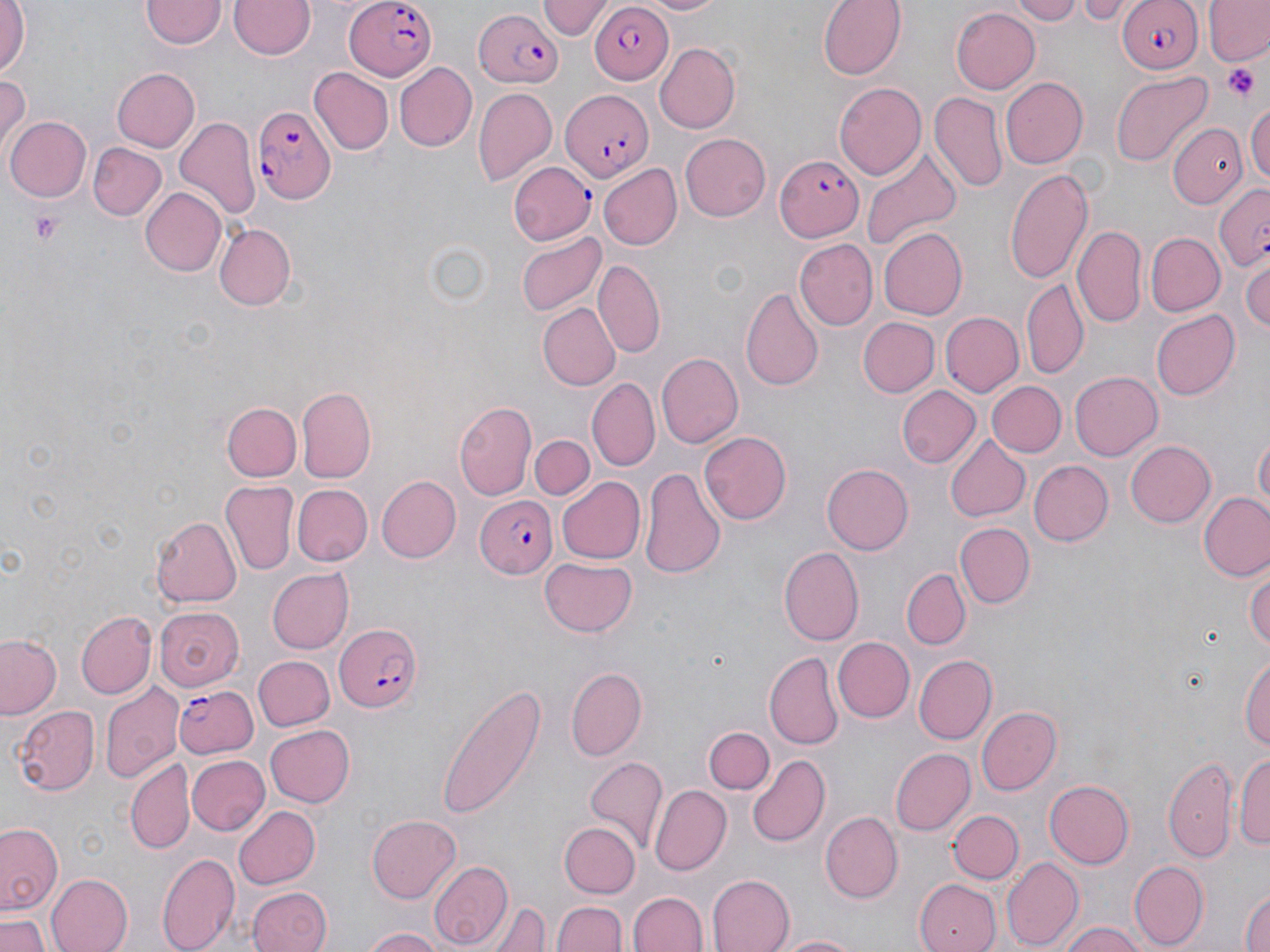
Approximate bounding boxes as (x1,y1)-(x2,y2) corner pairs in pixels. Plasmodium falciparum-infected red blood cell locations: (345,0)-(438,80), (1114,0)-(1203,74), (588,5)-(671,84), (473,8)-(563,90), (560,91)-(653,179), (252,107)-(336,204), (774,155)-(862,241), (508,163)-(593,246), (1212,182)-(1270,272), (472,494)-(558,579), (332,621)-(421,713), (172,685)-(258,757). Platelet locations: (1222,64)-(1260,101), (30,210)-(65,245). Uninfected red blood cell locations: (635,0)-(726,16), (818,0)-(907,80), (1004,0)-(1084,23), (1073,0)-(1133,25), (1204,0)-(1270,65), (229,1)-(315,60), (537,1)-(610,41), (0,2)-(29,78), (141,2)-(224,50), (951,6)-(1039,94), (653,41)-(739,134), (392,61)-(477,152), (310,67)-(392,153), (111,68)-(200,153), (1111,71)-(1214,167), (0,74)-(29,152), (1001,76)-(1088,169), (3,78)-(46,175), (835,80)-(928,180), (474,87)-(557,188), (930,91)-(1006,192), (1247,98)-(1270,187), (6,116)-(91,201), (175,119)-(259,221), (1170,123)-(1248,209), (680,134)-(772,222), (89,143)-(166,221), (862,147)-(962,247), (598,164)-(681,249), (1004,164)-(1092,286), (138,187)-(227,277), (215,223)-(295,308), (1072,224)-(1147,328), (880,227)-(967,319), (516,231)-(606,318), (1146,233)-(1223,317), (793,239)-(876,330), (1241,257)-(1270,335), (593,261)-(664,359), (1023,278)-(1088,380), (742,288)-(824,393), (536,303)-(620,391), (1152,311)-(1241,399), (941,312)-(1022,396), (856,317)-(939,396), (658,352)-(743,448), (1069,370)-(1163,459), (588,378)-(660,471), (986,382)-(1064,456), (897,386)-(981,468), (298,389)-(377,484), (221,402)-(301,482), (455,402)-(537,499), (700,431)-(793,524), (1253,432)-(1269,516), (529,435)-(595,500), (946,437)-(1029,522), (1126,440)-(1217,527), (1027,459)-(1113,547), (822,463)-(913,554), (640,467)-(726,578), (374,475)-(461,563), (555,477)-(645,565), (222,481)-(297,575), (293,485)-(371,566), (1199,491)-(1270,582), (150,515)-(242,607), (955,521)-(1034,608), (777,545)-(864,646), (539,556)-(639,638), (1247,563)-(1270,656), (265,567)-(353,654), (902,568)-(969,648), (153,605)-(244,689), (76,611)-(157,699), (0,634)-(64,720), (833,637)-(915,722), (765,652)-(843,749), (915,654)-(997,743), (251,655)-(334,732), (1241,655)-(1270,755), (566,666)-(647,762), (100,682)-(181,783), (435,685)-(545,820), (11,703)-(101,796), (978,707)-(1061,795), (265,724)-(355,806), (703,724)-(775,794), (891,748)-(975,836), (1235,749)-(1270,853), (186,754)-(269,837), (748,754)-(831,847), (1164,754)-(1239,864), (126,758)-(194,853), (585,758)-(668,853), (1043,779)-(1133,869), (648,784)-(732,876), (233,804)-(320,889), (948,809)-(1023,884), (821,812)-(903,902), (366,813)-(460,904), (559,821)-(639,897), (0,823)-(63,917), (556,840)-(630,952), (158,848)-(239,952), (1002,856)-(1081,949), (428,859)-(511,949), (1129,860)-(1206,948), (46,871)-(131,952), (708,872)-(795,952), (915,876)-(1001,952), (1240,884)-(1270,952), (248,887)-(330,952), (631,890)-(708,952), (554,900)-(625,952), (490,901)-(550,952), (0,915)-(48,952), (1061,922)-(1147,952), (361,927)-(449,952), (770,932)-(869,952). Slide-level diagnosis: Plasmodium falciparum. Optical microscopy. May-Grünwald-Giemsa-stained preparation. Single field of view. Image is 1270×952 pixels. 1000x magnification. Thin blood film.